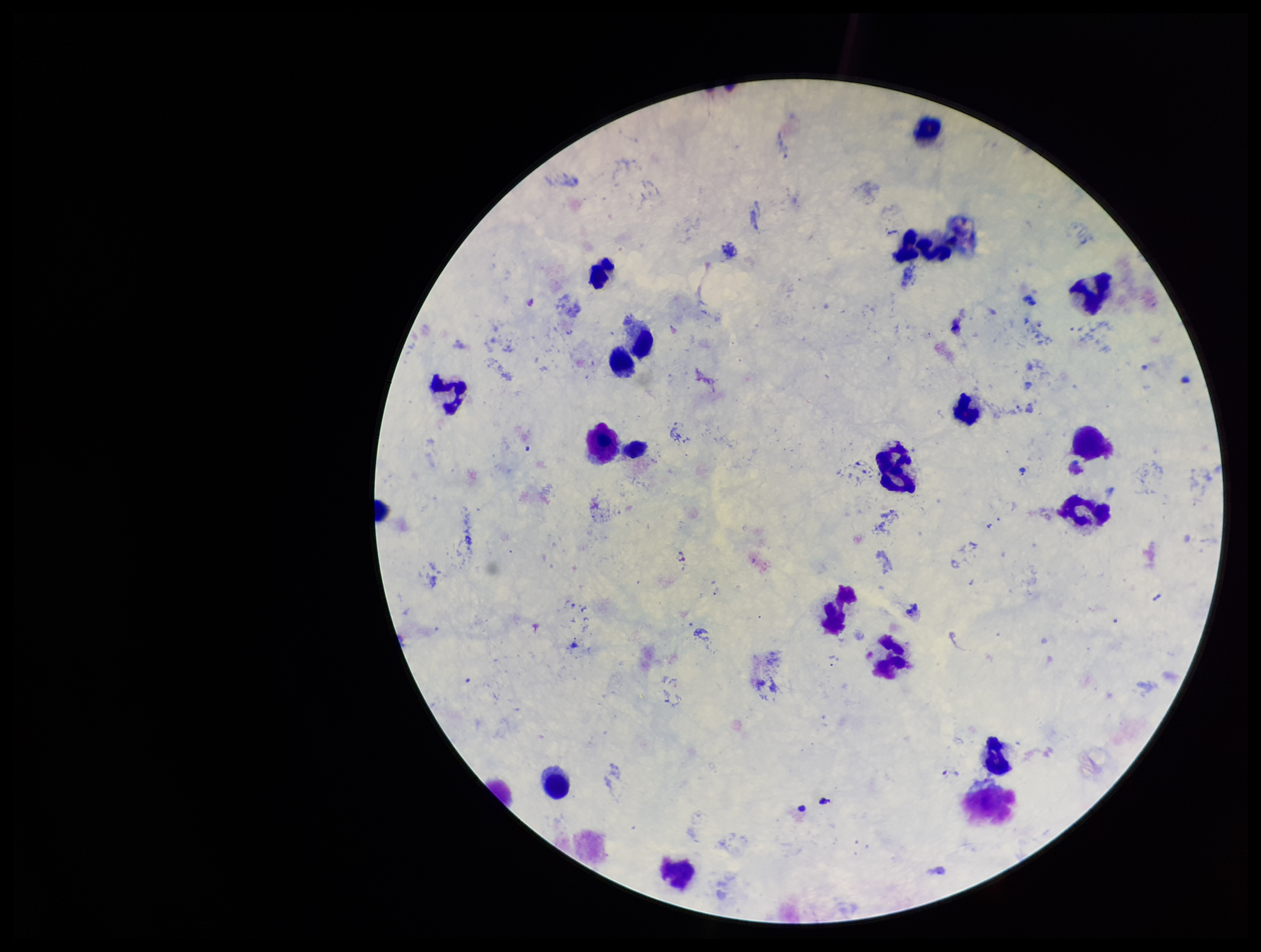
Summary:
  - Patient malaria status: infected
  - Species reported for this patient: Plasmodium vivax
  - Capture: smartphone photograph through the microscope eyepiece
  - Stain: Giemsa
  - Plasmodium parasites: none identified
  - Image size: 1261×952 pixels
  - Parasite count: 0
  - Field of view: one from this slide
  - Preparation: thick
  - Leukocyte count: 16